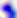

Summary:
  - Magnification: 400x
  - Identification: Toxoplasma gondii
  - Modality: micrograph